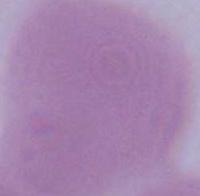

Summary:
  - Magnification: 1000x
  - Identification: red blood cell
  - Modality: photomicrograph